Assess this cell for malaria.
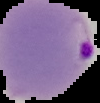

Parasitized.

Cell region segmented out of the field of view; the surrounding area is masked to black. From a thin blood film. Image is 100×103 pixels.